State which parasite is depicted.
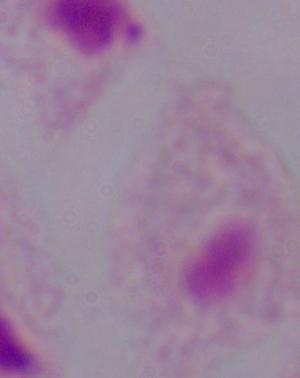
A trichomonad.

1000x magnification. Micrograph.